Assess this cell for malaria.
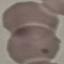
It is uninfected.

preparation: thin smear
capture: smartphone camera at the microscope eyepiece
stain: Giemsa
image_type: cell patch, automatically extracted from a larger field of view and resized to 64 × 64 pixels